Report the malaria status of this cell.
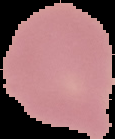

Uninfected.

Summary:
  - Preparation: thin blood smear
  - Image type: segmented cell region with the area outside set to black
  - Image size: 115×139 pixels